Comment on the morphology of the red blood cells.
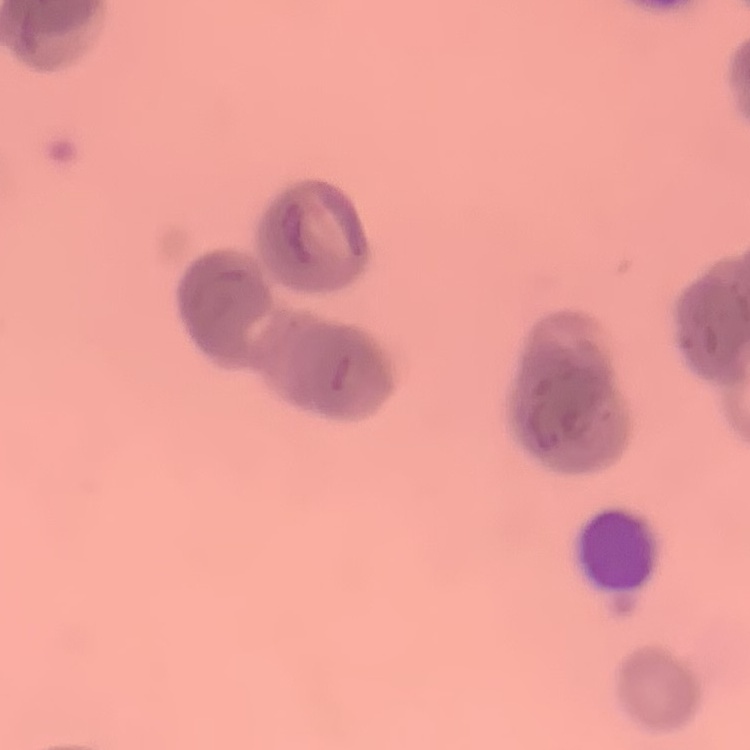
They show rouleaux formation.

Summary:
  - Image type: one tile cut from a larger photomicrograph
  - Preparation: thin peripheral smear
  - Stain: Field's or Giemsa